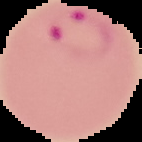
result = malaria parasites identified
image type = segmented cell region on a black background
preparation = thin blood film
image size = 142×142 pixels